Identify the parasite.
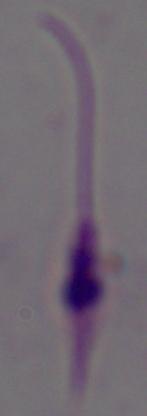

Leishmania.

Summary:
  - Modality: micrograph
  - Magnification: 1000x